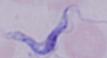

magnification = 1000x
modality = photomicrograph
identification = trypanosome